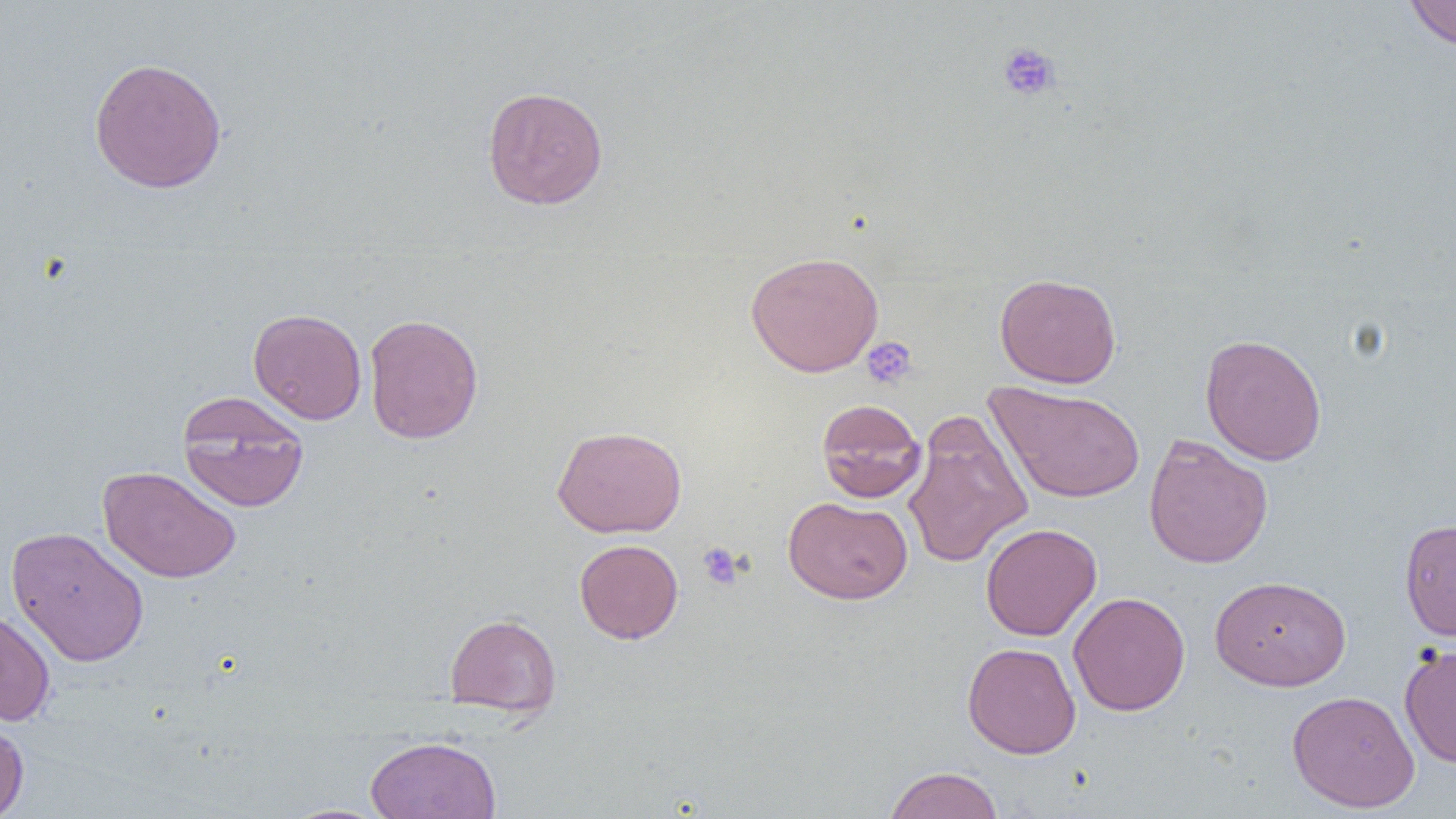
slide-level diagnosis = no evidence of blood parasites
preparation = thin blood smear
image size = 1456×819 pixels
magnification = 1000x
uninfected red blood cell locations = approximate bounding boxes as (x1,y1)-(x2,y2) corner pairs in pixels: (1403,0)-(1456,51), (88,56)-(228,194), (482,86)-(609,210), (745,251)-(885,377), (995,272)-(1121,388), (248,308)-(367,424), (363,313)-(483,444), (1200,333)-(1327,466), (985,380)-(1146,503), (177,391)-(309,513), (816,398)-(926,503), (902,414)-(1033,569), (552,425)-(687,538), (1143,434)-(1273,569), (98,465)-(241,583), (784,496)-(913,604), (1399,517)-(1456,641), (980,523)-(1102,641), (6,525)-(149,667), (574,539)-(683,644), (1209,575)-(1351,691), (1068,591)-(1191,716), (0,610)-(55,726), (444,612)-(561,718), (962,642)-(1081,759), (1399,642)-(1456,769), (1287,689)-(1420,812), (0,717)-(29,819), (365,736)-(502,819), (884,766)-(1003,819), (278,803)-(395,819)
field of view = single
platelet locations = approximate bounding boxes as (x1,y1)-(x2,y2) corner pairs in pixels: (997,41)-(1061,102), (861,337)-(918,390), (697,541)-(745,590)
modality = light microscopy